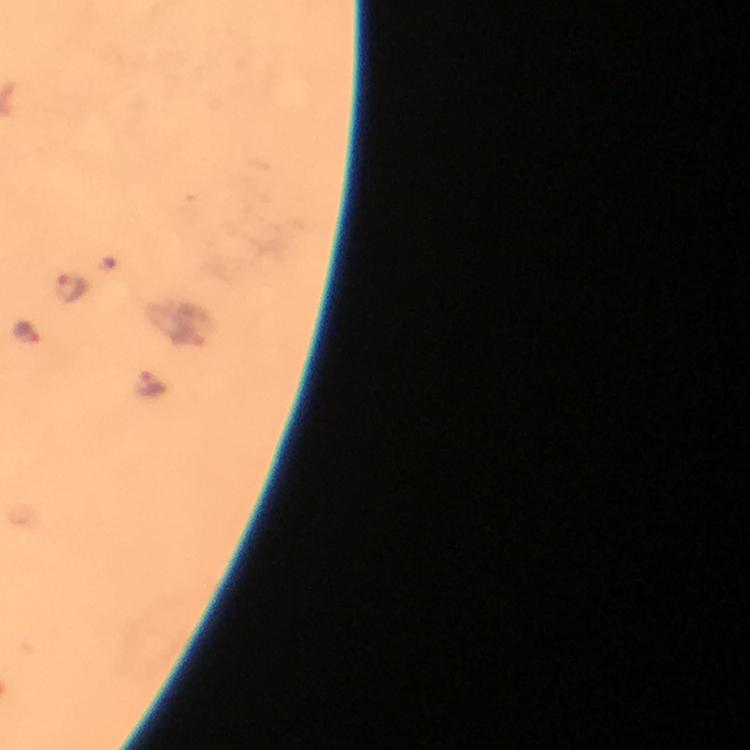
Approximate centers as {x, y} in pixels. Malaria parasite locations: {69, 288}, {25, 331}, {151, 382}. Immersion oil was used. Thick blood smear. A crop from one field of view. Photographed with a smartphone mounted on the microscope. Giemsa-stained preparation. Image is 750×750 pixels. 100x magnification. From a malaria diagnostic workup.